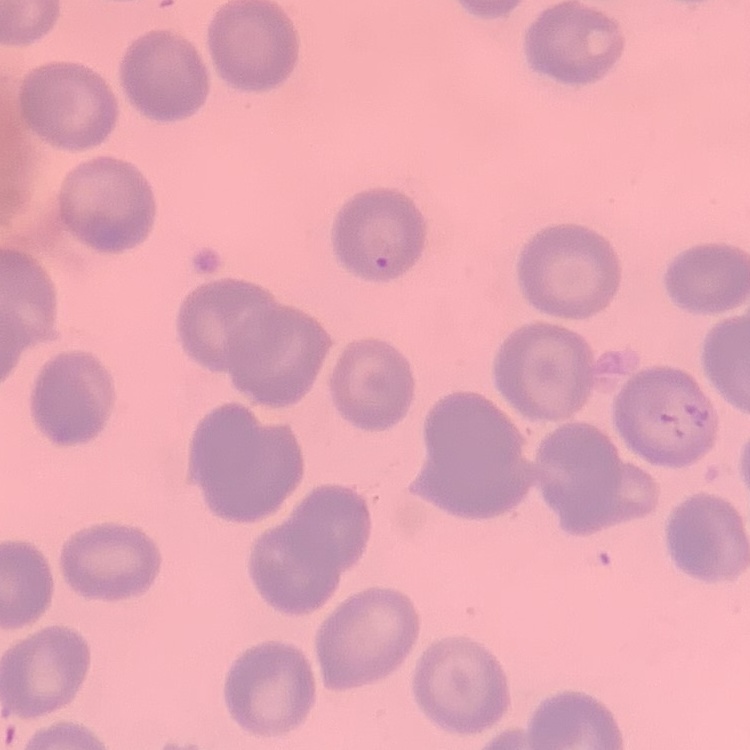

erythrocyte morphology = no rouleaux formation
preparation = thin blood smear
image type = one tile cut from a larger photomicrograph
stain = Field's or Giemsa